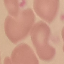
malaria status = uninfected
capture = smartphone camera at the microscope eyepiece
image type = cell patch, automatically extracted from a larger field of view and resized to 64 × 64 pixels
stain = Giemsa
preparation = thin blood film